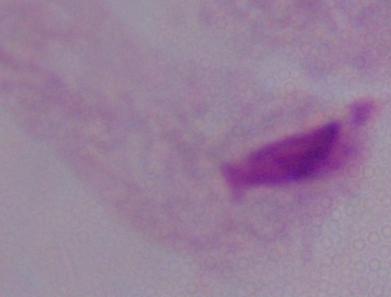
Summary:
  - Identification: trichomonad
  - Magnification: 1000x
  - Modality: photomicrograph